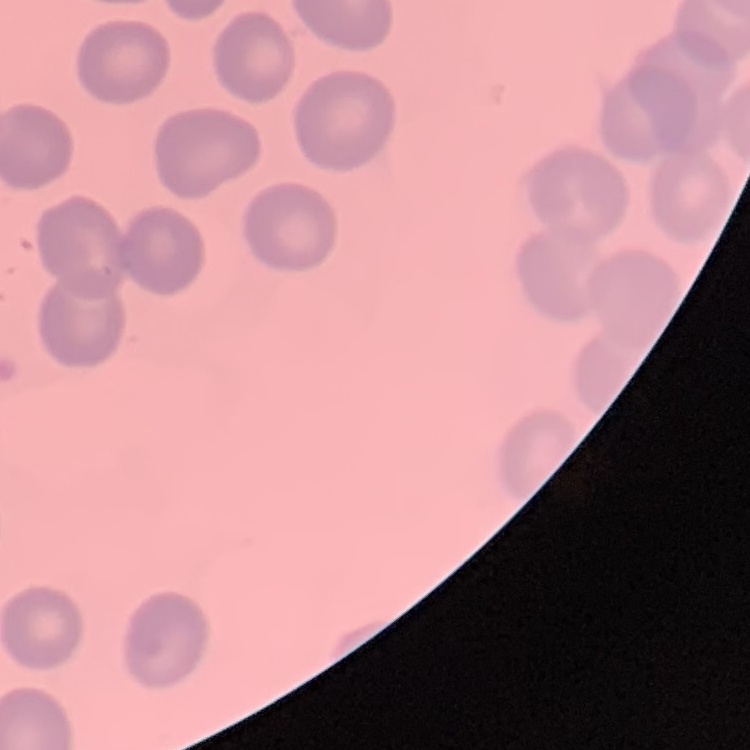
The red blood cells exhibit no rouleaux formation. Square crop of a larger photomicrograph. Thin peripheral smear. Field's or Giemsa stain.